Name the parasite shown.
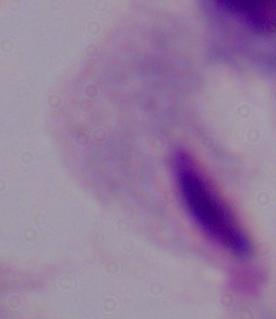

This is a trichomonad.

modality = micrograph
magnification = 1000x